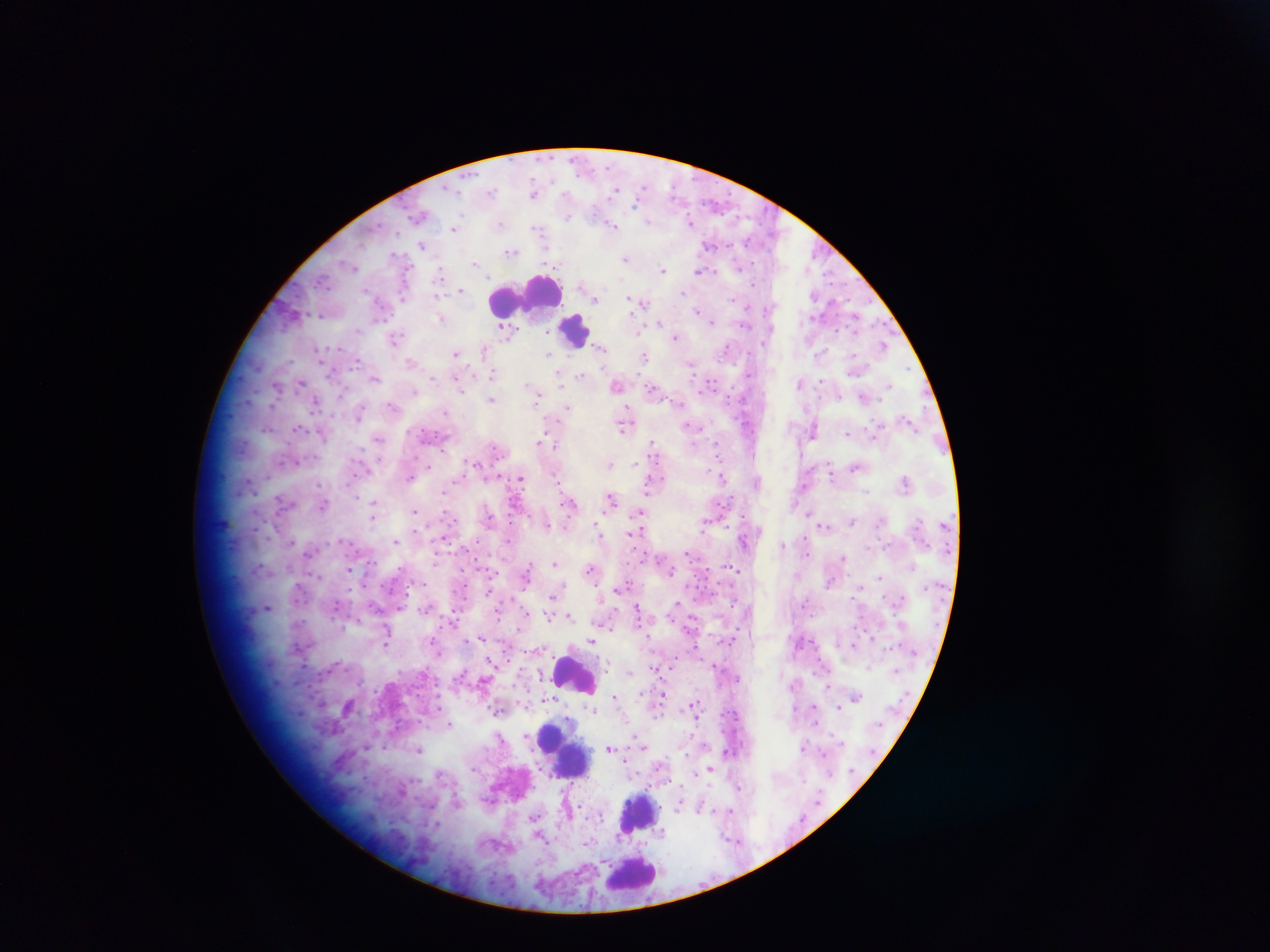

image size = 1270×952 pixels
country = Ghana
field of view = single
leukocyte locations = approximate centers as x y in pixels: 533 294; 575 329; 576 674; 551 737; 560 747; 572 757; 639 813; 632 874
preparation = thick blood smear
Plasmodium parasite locations = approximate centers as x y in pixels: 535 192; 419 216; 692 221; 613 224; 454 228; 710 244; 423 245; 511 251; 625 257; 474 264; 664 270; 702 270; 461 289; 683 291; 815 295; 595 298; 640 303; 442 317; 709 318; 660 322; 506 328; 677 336; 396 339; 884 345; 601 346; 727 348; 485 349; 457 353; 550 353; 645 357; 412 362; 691 362; 560 372; 492 374; 582 375; 375 378; 302 382; 802 383; 890 383; 277 385; 616 385; 653 388; 535 392; 865 397; 491 398; 316 404; 393 405; 567 408; 360 413; 910 421; 624 425; 691 426; 297 427; 814 428; 848 433; 875 435; 379 439; 541 442; 653 442; 609 463; 857 466; 831 470; 722 476; 521 479; 757 480; 905 481; 652 483; 804 486; 612 498; 282 501; 570 502; 323 504; 374 505; 415 511; 641 513; 490 518; 853 520; 546 524; 824 526; 599 534; 634 534; 395 541; 783 544; 310 552; 844 558; 555 563; 591 568; 349 569; 737 569; 671 571; 880 575; 526 576; 831 581; 861 585; 624 586; 489 591; 553 596; 266 607; 400 607; 638 612; 549 615; 569 616; 387 634; 481 638; 592 640; 386 641; 853 644; 695 646; 492 661; 656 669; 829 684; 663 694; 616 696; 855 697; 348 706; 693 707; 838 707; 450 725; 502 738; 804 746; 610 747; 419 748; 625 760; 710 768; 730 811; 662 832; 540 837
capture = mobile-phone photograph through a microscope